Name the cell type shown.
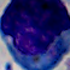
This is a leukocyte.

magnification: 1000x
modality: micrograph